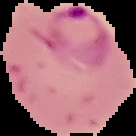

Image is 136×136 pixels. Cell region segmented out of the field of view; the surrounding area is masked to black. Result: malaria parasites detected. From a thin blood smear.